Give a bounding box for every leukocyte visible.
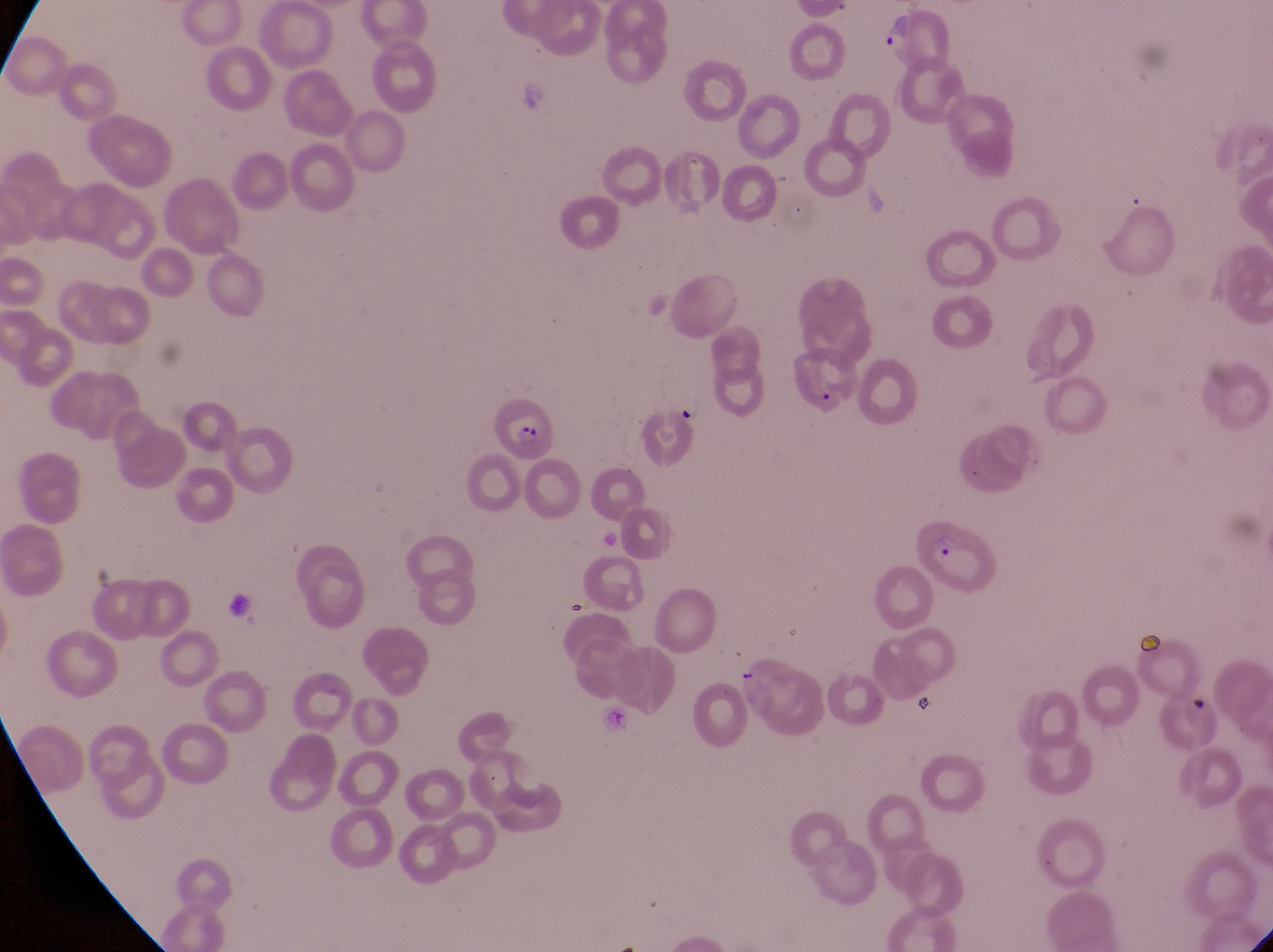

No leukocytes observed.

parasitised red blood cell locations = approximate bounding boxes as (left, top, right, bottom) in pixels: (789, 345, 871, 427), (497, 395, 555, 458), (917, 524, 999, 601)
preparation = thin blood smear
artifact (platelet-like body, stain precipitate, or debris) locations = approximate bounding boxes as (left, top, right, bottom) in pixels: (1133, 621, 1168, 658), (909, 684, 936, 723)
image size = 1273×952 pixels
field of view = single
capture = smartphone photograph through the eyepiece of an Olympus CX-23 microscope
trophozoite locations = approximate bounding boxes as (left, top, right, bottom) in pixels: (866, 2, 913, 57), (672, 395, 707, 427)
magnification = 1000x
country = Uganda